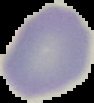

Summary:
  - Preparation: thin blood film
  - Image type: segmented cell region with the area outside set to black
  - Result: no Plasmodium parasites seen
  - Image size: 94×103 pixels